Locate every Plasmodium parasite.
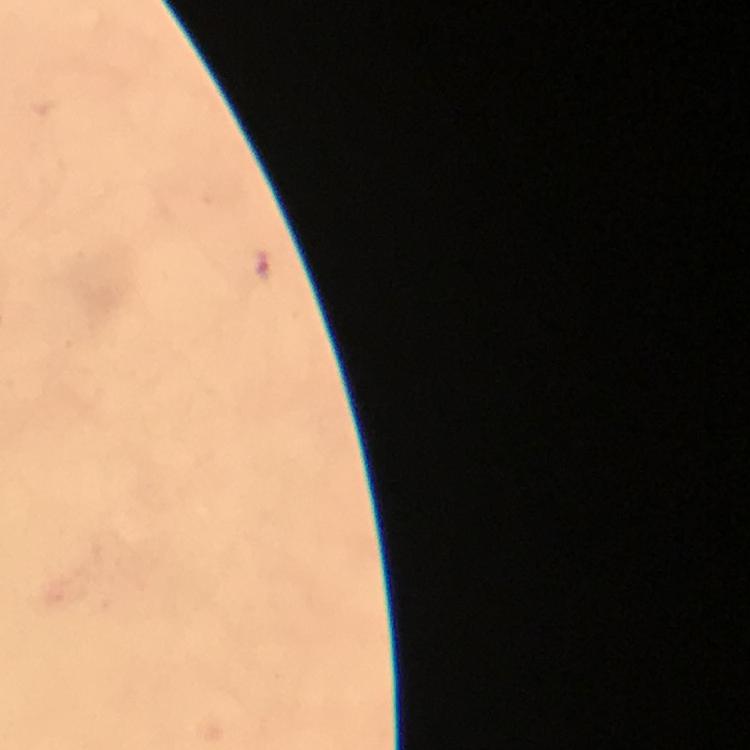
Approximate centers as {x, y} in pixels.
Plasmodium parasites: {261, 266}.

capture = smartphone mounted on the microscope
context = from a malaria diagnostic workup
preparation = thick blood film
magnification = 100x
image size = 750×750 pixels
immersion oil = used
cropped from = a single field of view
stain = Giemsa